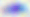

Summary:
  - Identification: Toxoplasma gondii
  - Modality: photomicrograph
  - Magnification: 400x